Point out each malaria parasite.
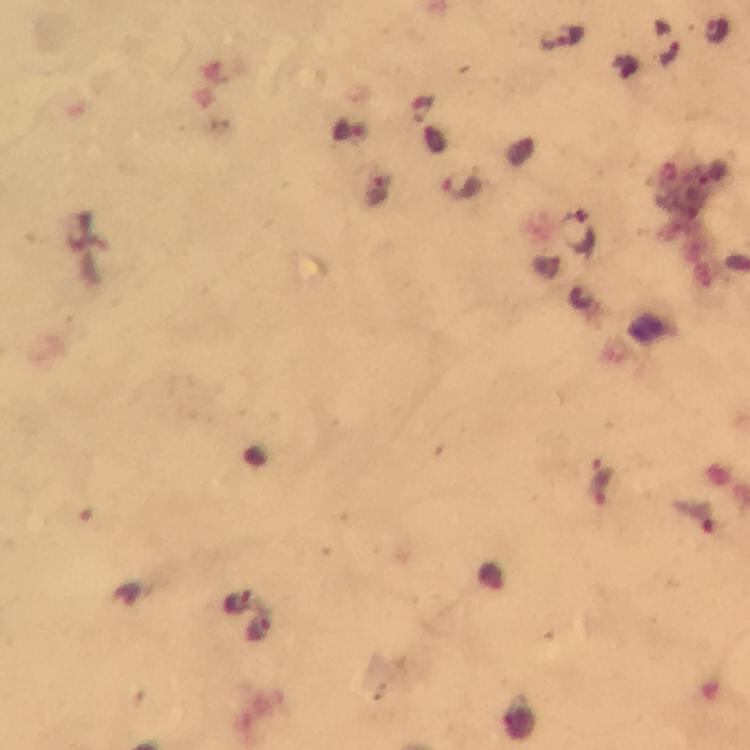
Approximate centers as (x, y) in pixels.
Malaria parasites: (561, 37), (463, 188), (579, 232).

100x magnification. From a diagnostic examination for malaria. Giemsa-stained preparation. Thick blood smear. A crop from one field of view. Immersion oil was used. Image is 750×750 pixels. Photographed through the microscope with a smartphone camera.